Assess this cell for malaria.
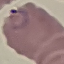
It is parasitized.

preparation = thin blood smear
capture = smartphone through the microscope eyepiece
image type = cell patch, automatically extracted from a larger field of view and resized to 64 × 64 pixels
stain = Giemsa